Outline each blood parasite and name the species.
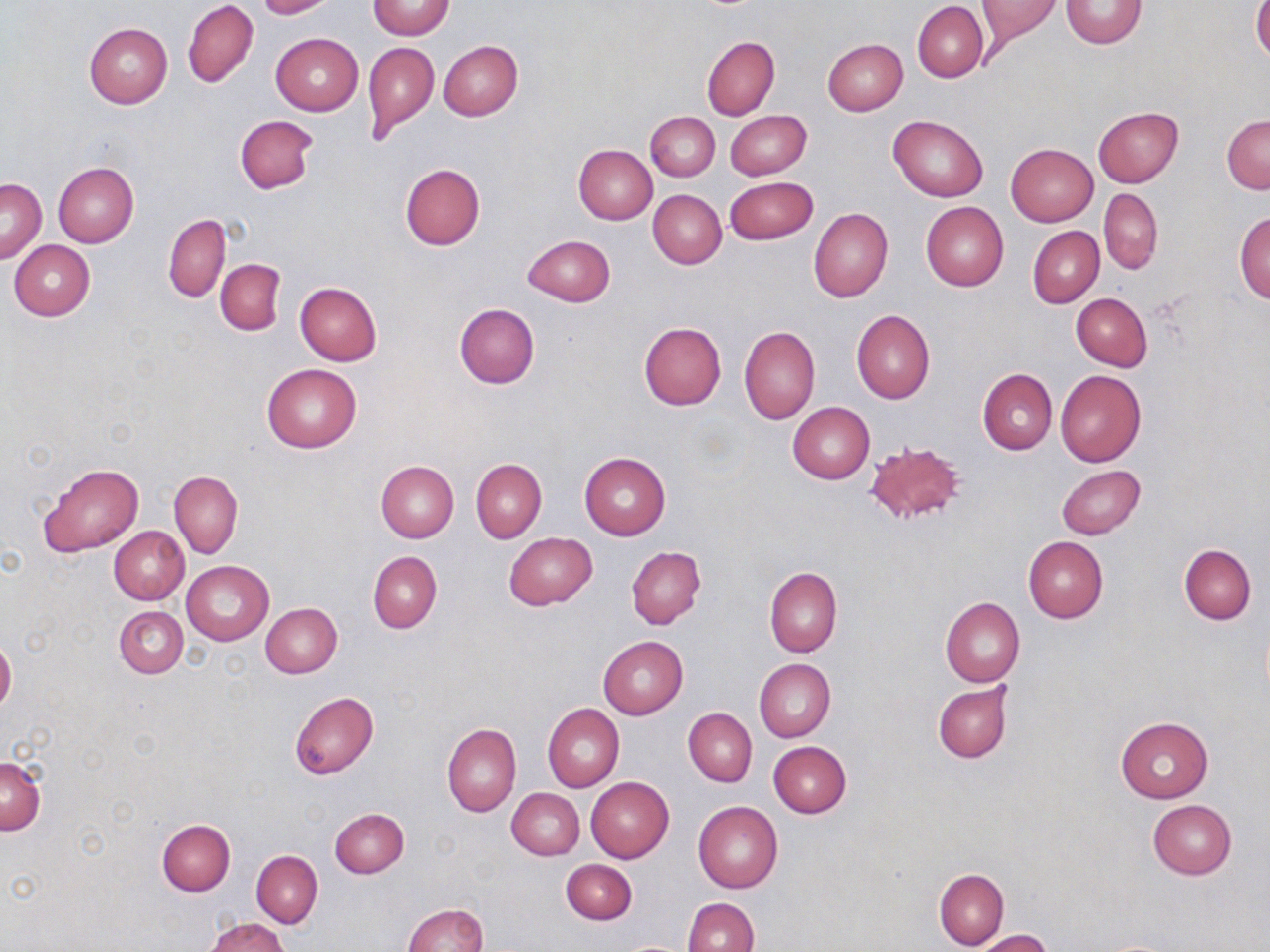
No blood parasites seen.

Approximate bounding boxes as (x1,y1)-(x2,y2) corner pairs in pixels. Uninfected red blood cell locations: (254,0)-(334,18), (975,0)-(1062,41), (1060,0)-(1147,49), (183,1)-(258,88), (368,1)-(454,39), (914,3)-(988,83), (1251,3)-(1270,64), (84,22)-(172,109), (271,33)-(363,116), (702,36)-(779,120), (822,38)-(908,115), (439,40)-(522,121), (363,41)-(439,143), (1093,107)-(1183,187), (725,110)-(811,179), (646,112)-(719,181), (234,115)-(319,194), (888,115)-(988,201), (1222,115)-(1269,194), (1006,143)-(1098,226), (573,145)-(657,224), (53,161)-(139,246), (400,164)-(484,250), (726,176)-(818,244), (1,177)-(45,264), (1099,188)-(1163,273), (648,189)-(727,269), (921,202)-(1008,291), (809,208)-(893,303), (1234,211)-(1270,305), (163,214)-(230,303), (1029,226)-(1104,307), (523,234)-(615,307), (9,240)-(94,321), (216,260)-(285,334), (294,282)-(382,366), (1071,293)-(1152,369), (454,303)-(539,388), (851,309)-(935,404), (639,321)-(727,410), (740,327)-(820,424), (262,363)-(362,452), (978,369)-(1057,454), (1055,370)-(1146,467), (787,402)-(874,483), (865,441)-(967,528), (579,452)-(670,541), (471,459)-(546,542), (375,460)-(459,542), (39,462)-(143,556), (1056,465)-(1145,540), (170,470)-(242,557), (133,482)-(237,578), (108,526)-(189,605), (504,533)-(596,610), (1023,536)-(1109,623), (1179,543)-(1255,623), (627,546)-(705,629), (368,551)-(441,633), (181,561)-(273,645), (765,566)-(842,657), (939,596)-(1024,686), (260,602)-(342,678), (115,605)-(188,678), (598,635)-(688,719), (0,639)-(16,713), (755,658)-(835,742), (933,684)-(1011,762), (288,691)-(380,779), (543,704)-(624,793), (684,708)-(757,787), (1115,716)-(1212,802), (442,723)-(521,817), (768,741)-(852,818), (0,756)-(46,835), (586,777)-(675,862), (507,788)-(583,859), (693,800)-(783,892), (1148,800)-(1237,879), (329,808)-(409,878), (158,819)-(234,896), (252,850)-(322,927), (561,859)-(636,925), (934,869)-(1009,949), (683,898)-(759,952), (402,903)-(488,952), (206,917)-(290,952), (976,929)-(1054,952). Slide-level diagnosis: no evidence of blood parasites. Single field of view. May-Grünwald-Giemsa stain. Thin blood film. Image is 1270×952 pixels. Light microscopy. Captured at 1000x magnification.